Report the malaria status of this cell.
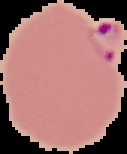
Parasitized.

From a thin blood smear. Image is 127×154 pixels. Cell region segmented out of the field of view; the surrounding area is masked to black.